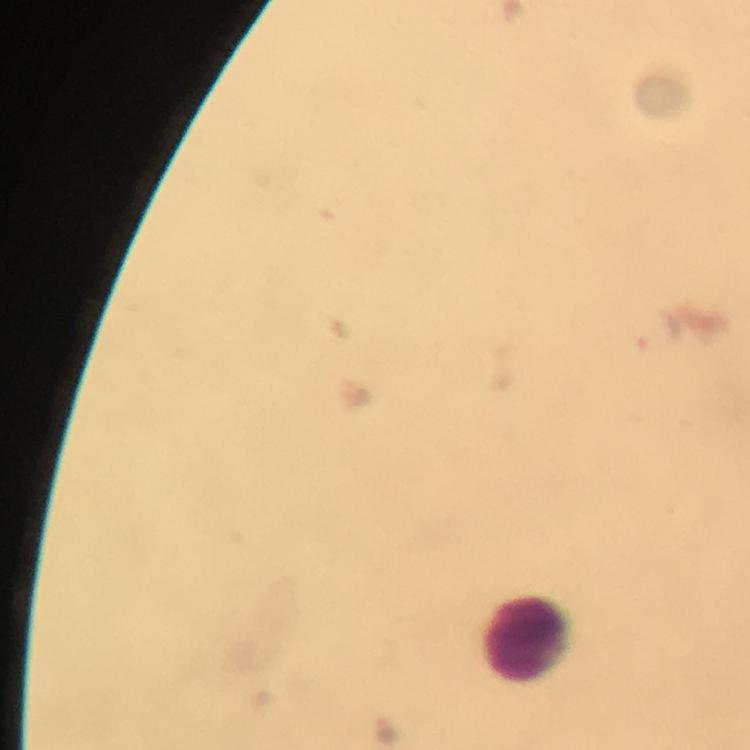

Approximate centers as (x, y) in pixels.
Summary:
  - Leukocyte locations: (528, 640)
  - Plasmodium parasite locations: (656, 331)
  - Immersion oil: applied
  - Cropped from: a single field of view
  - Magnification: 100x
  - Context: from a malaria diagnostic workup
  - Preparation: thick blood film
  - Image size: 750×750 pixels
  - Stain: Giemsa
  - Capture: smartphone mounted on the microscope